Report the malaria status of this cell.
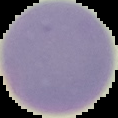
Uninfected.

image size = 118×118 pixels
preparation = thin blood film
image type = segmented cell region on a black background